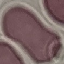

result = no malaria parasites detected
preparation = thin smear
stain = Giemsa
image type = automatically extracted cell patch, resized to 64 × 64 pixels
capture = smartphone through the microscope eyepiece